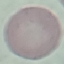 Malaria status: uninfected. Giemsa-stained preparation. Automatically extracted cell patch, resized to 64 × 64 pixels. Thin blood smear. Acquired by smartphone through the microscope eyepiece.